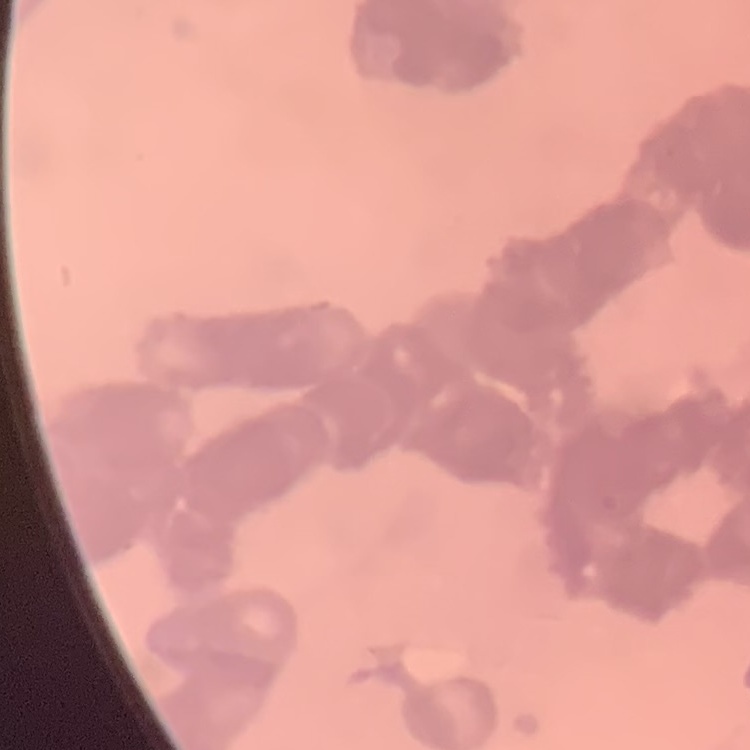
The erythrocytes exhibit rouleaux formation. Square crop of a larger photomicrograph. Thin blood film. Stained with either Field's or Giemsa.